Give the position of every leukocyte visible.
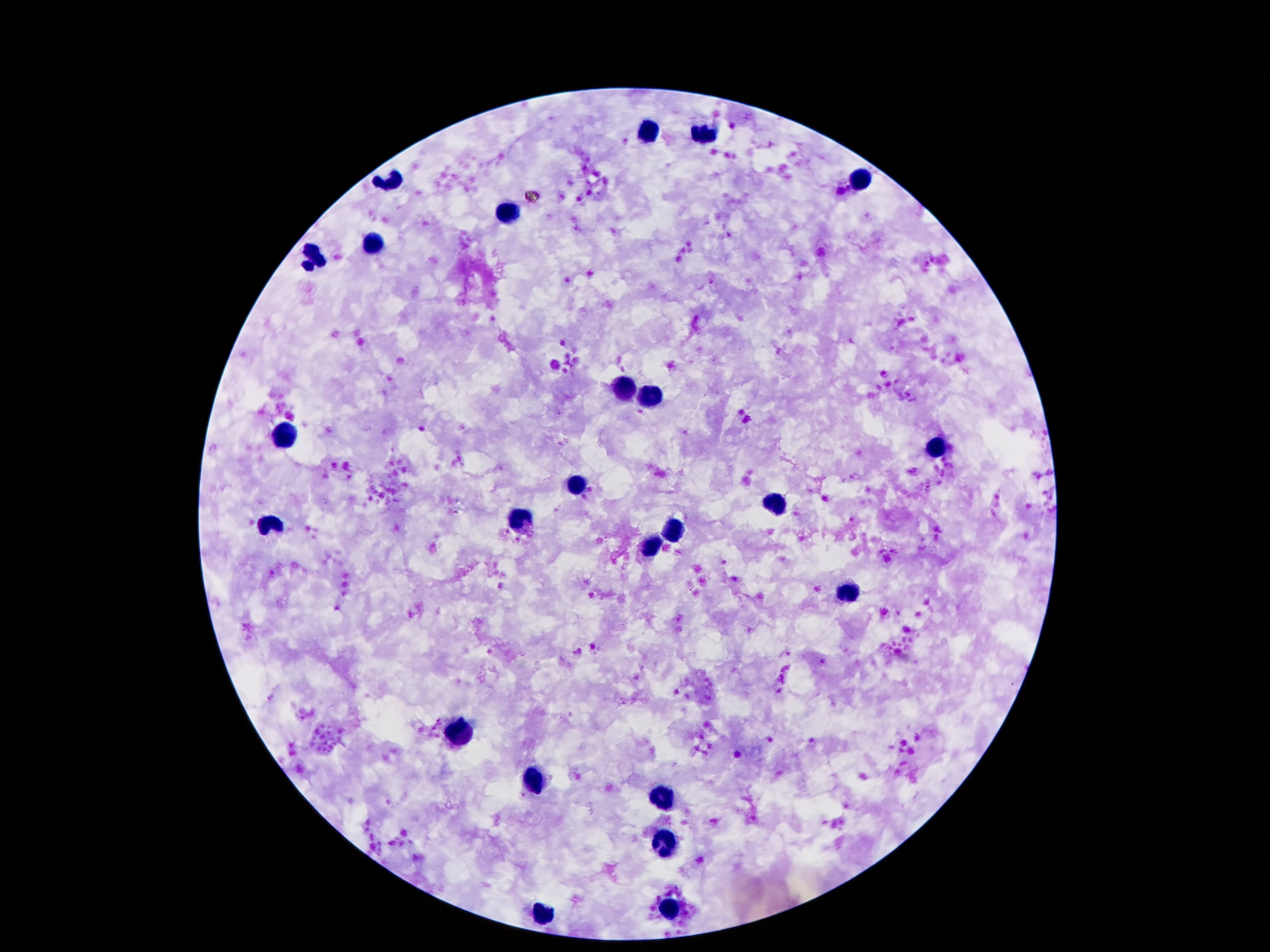
Approximate centers as [x, y] in pixels.
Leukocytes: [646, 134], [702, 135], [387, 182], [863, 184], [505, 212], [370, 241], [310, 257], [627, 388], [651, 397], [284, 435], [935, 448], [577, 486], [776, 505], [522, 520], [272, 527], [675, 527], [654, 546], [848, 594], [464, 733], [536, 778], [666, 800], [663, 839], [670, 908], [546, 913].

patient_malaria_status: uninfected
magnification: 100x
capture: smartphone camera through the microscope eyepiece
preparation: thick blood film
field_of_view: single
image_size: 1270×952 pixels
stain: Giemsa